Give the extent of all Trypanosoma brucei.
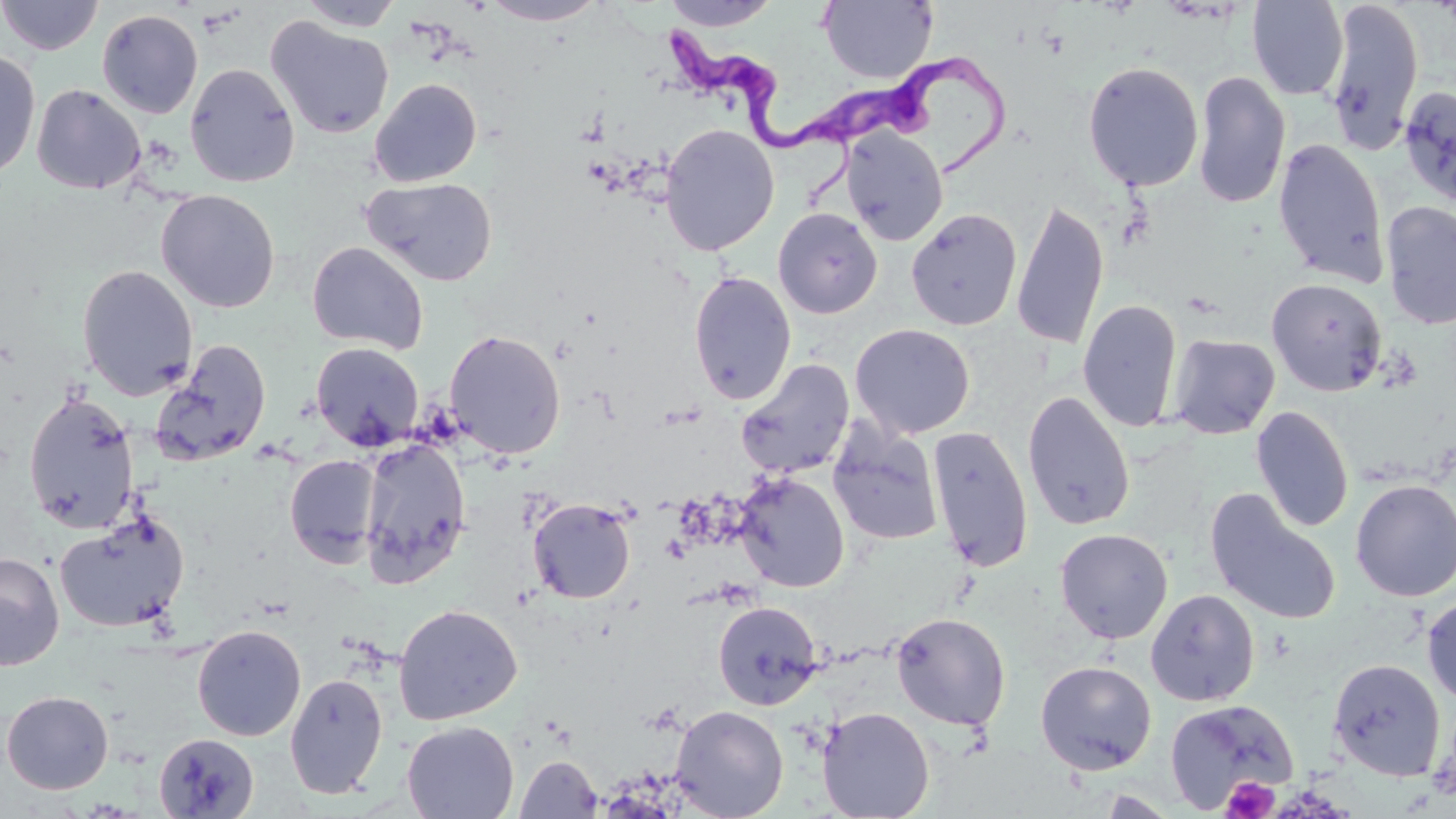
Approximate bounding boxes as (x1, y1, x2, y2) in pixels.
Trypanosoma brucei: (662, 30, 859, 199), (816, 43, 1018, 180).

Summary:
  - Platelet locations: (1220, 776, 1279, 819)
  - Uninfected red blood cell locations: (0, 0, 104, 56), (297, 0, 405, 31), (480, 0, 609, 25), (661, 0, 781, 31), (1246, 0, 1349, 100), (1324, 0, 1424, 154), (818, 1, 938, 83), (96, 9, 203, 118), (265, 16, 395, 139), (0, 48, 41, 181), (1082, 60, 1204, 192), (185, 63, 300, 187), (1192, 70, 1291, 209), (369, 77, 482, 187), (31, 84, 145, 194), (1398, 85, 1456, 208), (660, 124, 779, 256), (841, 127, 948, 246), (1273, 138, 1390, 288), (362, 176, 497, 286), (156, 189, 280, 313), (1011, 199, 1110, 353), (1381, 201, 1456, 330), (773, 207, 883, 319), (906, 209, 1022, 331), (306, 241, 429, 355), (77, 264, 198, 400), (688, 271, 796, 406), (1266, 278, 1387, 396), (1077, 299, 1183, 433), (850, 323, 975, 439), (444, 329, 566, 459), (1167, 334, 1280, 439), (152, 341, 273, 466), (311, 342, 424, 451), (735, 359, 855, 481), (23, 391, 140, 534), (1022, 391, 1135, 531), (1251, 406, 1354, 533), (828, 424, 944, 546), (926, 426, 1034, 572), (358, 439, 471, 588), (285, 455, 384, 568), (734, 472, 849, 593), (1350, 479, 1456, 601), (1205, 488, 1341, 626), (527, 498, 636, 603), (54, 514, 189, 634), (1055, 528, 1173, 643), (0, 552, 64, 671), (1145, 588, 1259, 706), (1421, 593, 1456, 709), (712, 601, 823, 710), (393, 604, 522, 726), (891, 612, 1011, 730), (192, 624, 306, 741), (1329, 657, 1445, 780), (1035, 660, 1157, 775), (285, 672, 388, 799), (1, 689, 114, 794), (1165, 699, 1298, 813), (670, 704, 789, 819), (817, 706, 935, 819), (402, 720, 519, 819), (152, 733, 259, 818), (515, 755, 603, 818), (1092, 790, 1183, 818)
  - Slide-level diagnosis: Trypanosoma brucei
  - Magnification: 1000x
  - Field of view: single
  - Modality: optical microscopy
  - Preparation: thin blood smear
  - Stain: May-Grünwald-Giemsa
  - Image size: 1456×819 pixels